Classify this cell by malaria status.
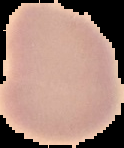
Uninfected.

image type = segmented cell region with the area outside set to black
preparation = thin blood film
image size = 124×148 pixels